Give the preparation type.
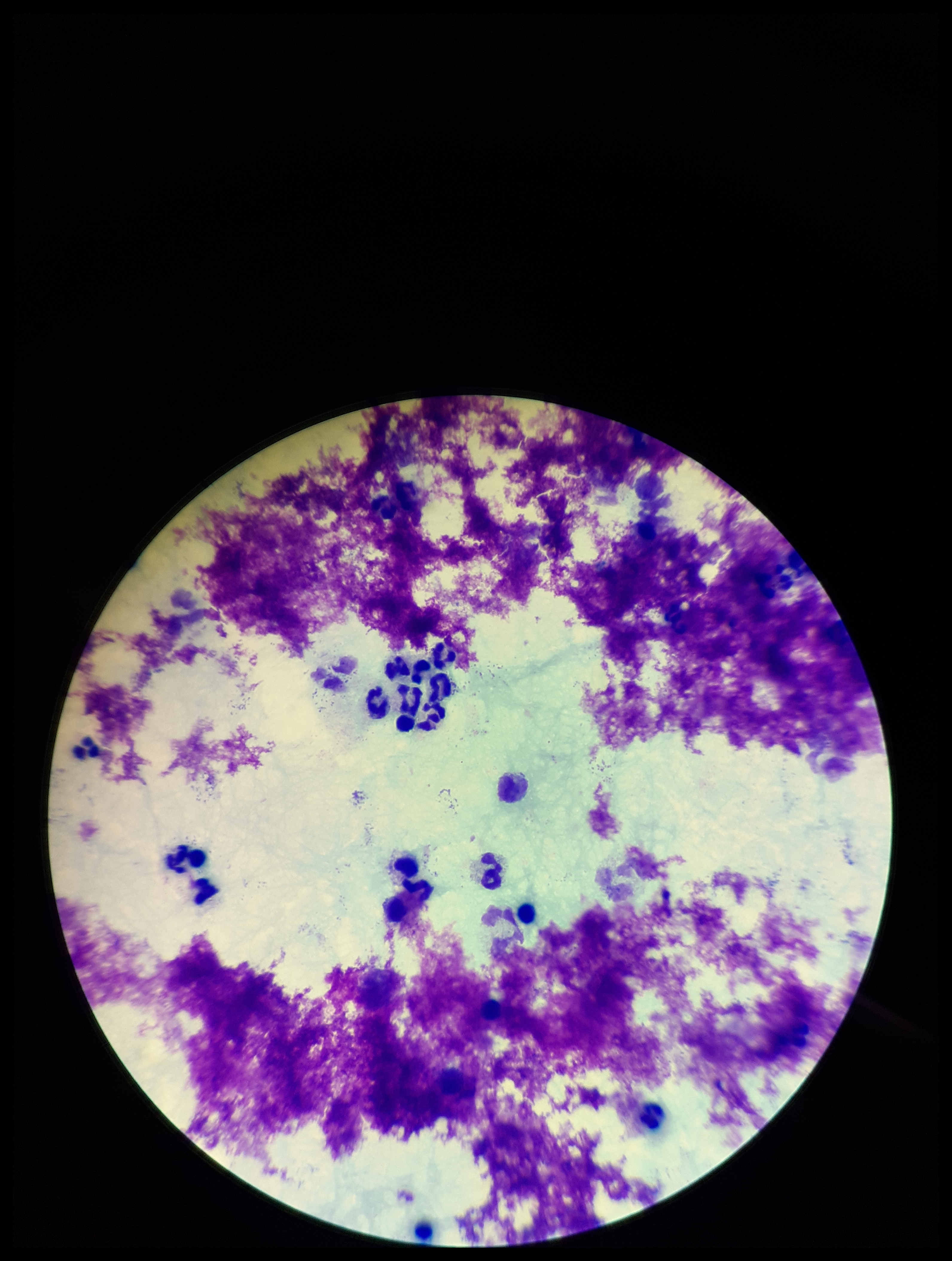

It is a thick blood smear.

parasite count = 0
image size = 952×1261 pixels
field of view = one from this slide
stain = Giemsa
Plasmodium parasites = none detected
capture = smartphone photograph through the microscope eyepiece
leukocyte count = 18
patient malaria status = negative